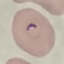
malaria status = parasitized
image type = automatically extracted cell patch, resized to 64 × 64 pixels
capture = smartphone camera at the microscope eyepiece
preparation = thin smear
stain = Giemsa